Locate every Plasmodium parasite.
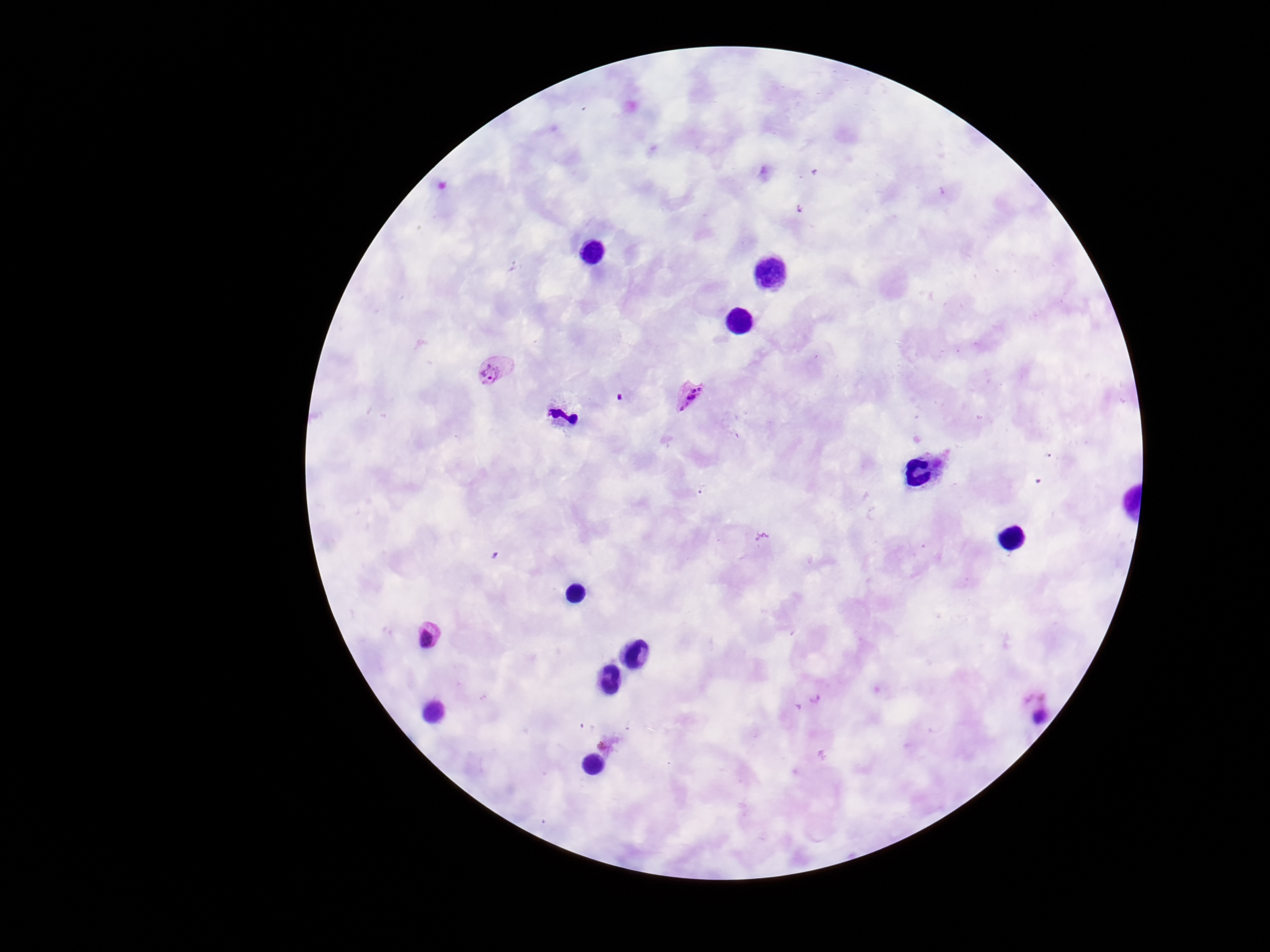

Approximate object centers, in pixels from the top-left corner.
Plasmodium parasites: (x=494, y=370), (x=690, y=396), (x=428, y=637), (x=607, y=745).

capture = smartphone camera through the microscope eyepiece
preparation = thick blood smear
image size = 1270×952 pixels
stain = Giemsa
patient malaria status = positive
field of view = one from this slide
magnification = 100x